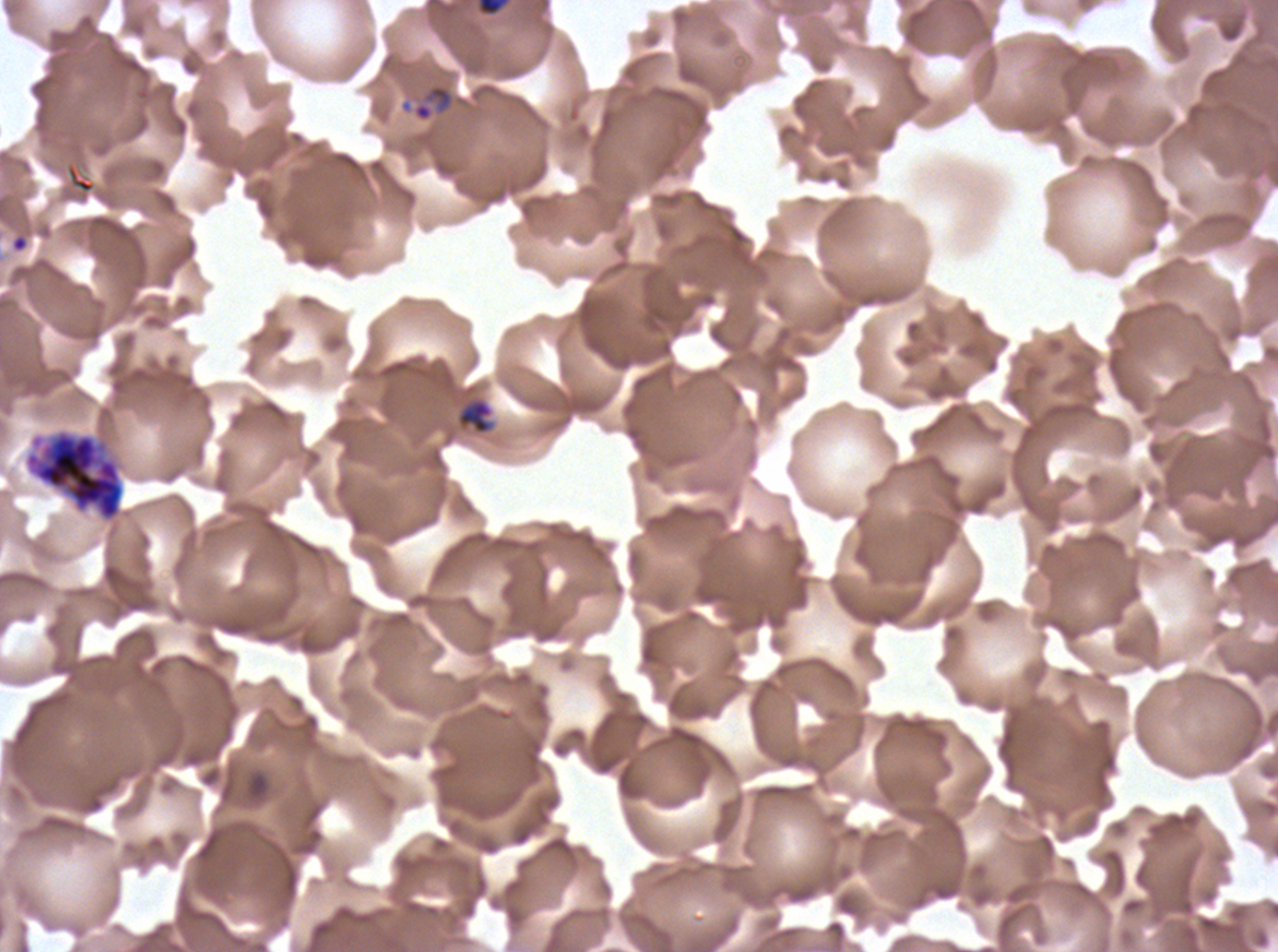
Approximate bounding boxes as (x1, y1, x2, y2) in pixels. Segmenter locations: (24, 429, 125, 522). Late-ring/early-trophozoite locations: (477, 0, 509, 16), (456, 398, 494, 435). Debris locations: (11, 235, 29, 252). Life-cycle stages observed: late-ring/early-trophozoite, segmenter. Ex-vivo P. falciparum culture from a patient in The Gambia, grown for 24 to 48 hours. Image is 1278×952 pixels. Giemsa stain. Thin blood smear. A sub-image separated from a larger composite.